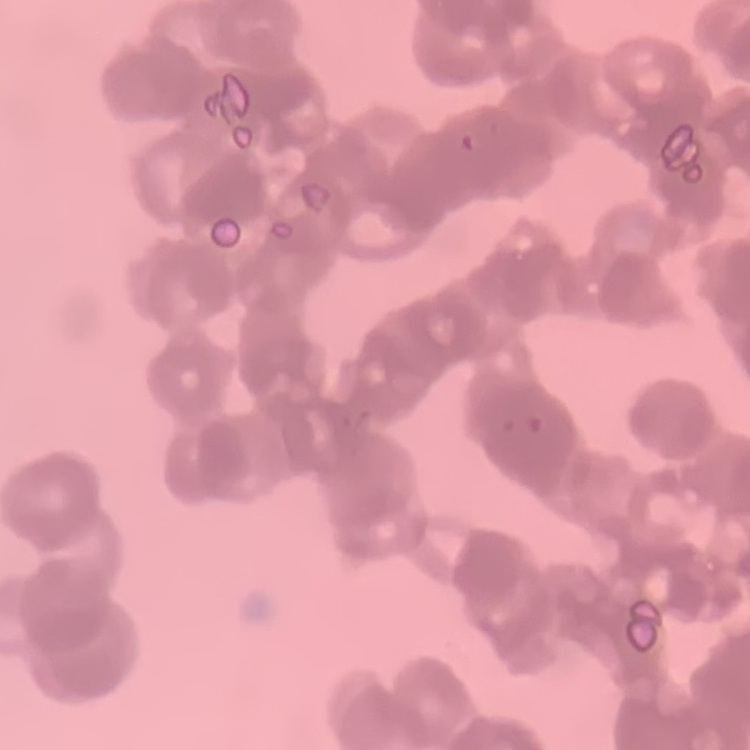

erythrocyte_morphology: rouleaux formation
stain: Field's or Giemsa
image_type: square crop of a larger photomicrograph
preparation: thin blood smear